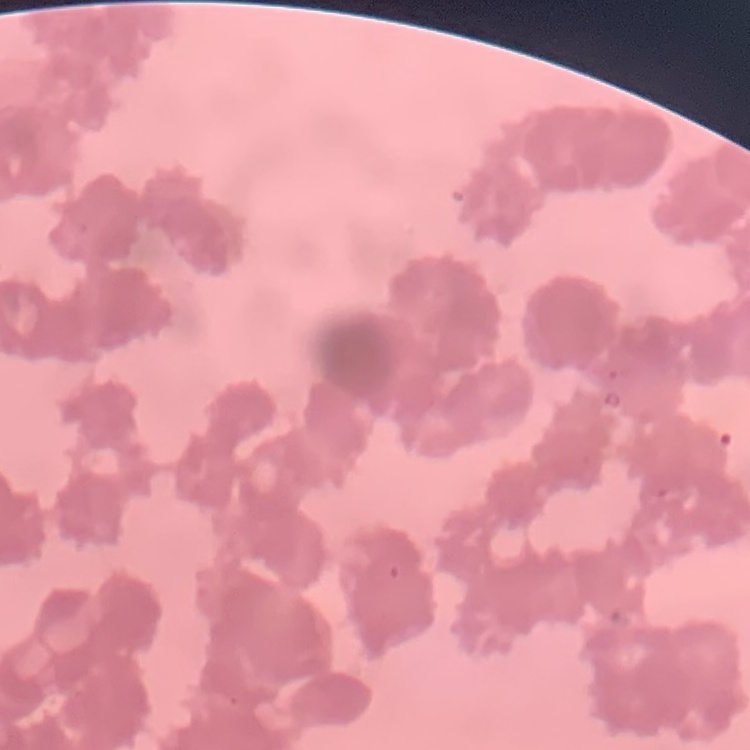

Summary:
  - Erythrocyte morphology: rouleaux formation
  - Preparation: thin blood film
  - Stain: Field's or Giemsa
  - Image type: one tile cut from a larger photomicrograph